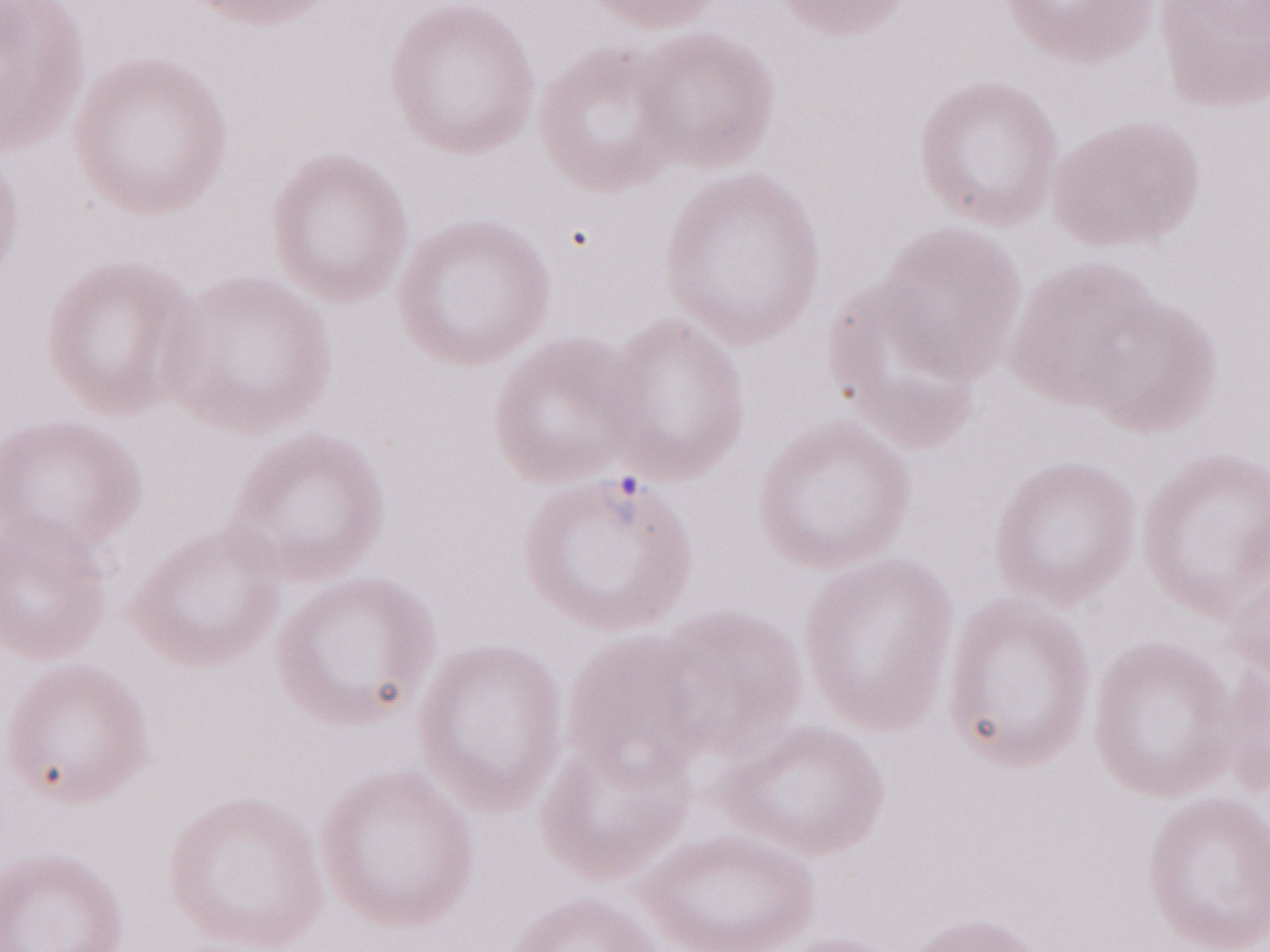

Patient-level malaria diagnosis: positive. May-Grünwald-Giemsa (MGG) stain. Image is 1270×952 pixels. One field of this slide. Olympus BX43 microscope, Olympus DP73 camera. Magnification: 1,000x. Thin blood smear.